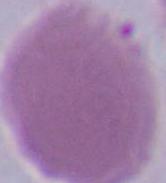

modality: photomicrograph
magnification: 1000x
identification: erythrocyte